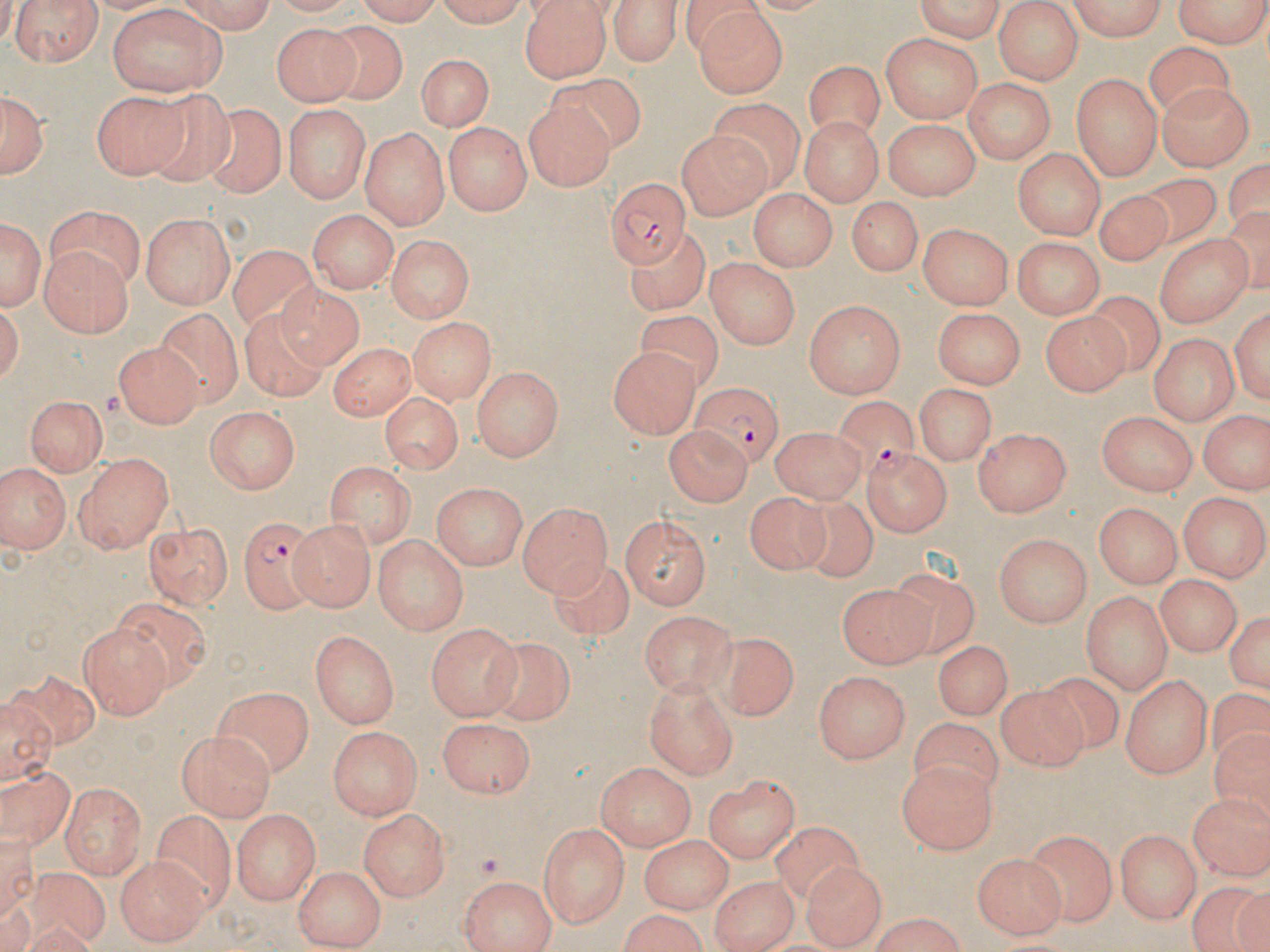 Approximate bounding boxes as [x1, y1, x2, y2] in pixels. Plasmodium falciparum-infected red blood cell locations: [604, 177, 691, 267], [691, 380, 782, 463], [835, 397, 930, 486], [855, 443, 951, 534], [238, 514, 317, 614]. Uninfected red blood cell locations: [6, 0, 106, 67], [172, 0, 278, 32], [349, 0, 451, 23], [429, 0, 531, 26], [519, 0, 610, 83], [607, 0, 686, 65], [906, 0, 1009, 41], [1060, 0, 1168, 41], [995, 1, 1080, 83], [1168, 1, 1270, 49], [692, 4, 788, 97], [107, 5, 226, 96], [315, 24, 408, 104], [270, 25, 356, 108], [882, 35, 980, 124], [1146, 45, 1235, 126], [416, 52, 492, 133], [805, 54, 884, 133], [543, 72, 652, 149], [1072, 74, 1164, 181], [963, 77, 1055, 164], [1157, 81, 1252, 173], [2, 87, 47, 178], [94, 90, 189, 180], [150, 91, 237, 190], [524, 95, 615, 192], [710, 98, 807, 195], [283, 103, 369, 204], [201, 105, 289, 203], [802, 117, 885, 205], [884, 118, 980, 200], [445, 121, 529, 216], [359, 126, 450, 225], [674, 129, 773, 217], [1015, 149, 1105, 239], [1144, 171, 1219, 248], [750, 190, 837, 270], [1091, 191, 1173, 266], [845, 199, 920, 279], [44, 203, 145, 288], [308, 210, 398, 295], [1, 213, 44, 311], [140, 216, 235, 309], [918, 224, 1015, 311], [1152, 234, 1256, 329], [386, 235, 475, 321], [626, 235, 714, 316], [1015, 237, 1104, 316], [227, 245, 327, 340], [39, 248, 132, 337], [706, 259, 803, 348], [277, 276, 377, 372], [1084, 291, 1174, 376], [803, 299, 901, 397], [1231, 301, 1269, 414], [240, 302, 328, 405], [932, 305, 1027, 388], [156, 310, 246, 406], [637, 311, 725, 396], [1039, 313, 1127, 396], [409, 317, 492, 404], [1148, 333, 1239, 423], [327, 339, 418, 418], [113, 344, 199, 429], [606, 345, 702, 437], [472, 366, 563, 461], [912, 382, 993, 464], [377, 392, 466, 471], [24, 393, 107, 478], [206, 406, 298, 495], [1097, 411, 1198, 495], [1200, 412, 1265, 494], [664, 424, 749, 507], [769, 428, 869, 500], [973, 428, 1072, 518], [72, 452, 178, 553], [2, 461, 70, 554], [328, 462, 417, 550], [428, 483, 529, 569], [1179, 491, 1267, 581], [746, 494, 833, 577], [794, 494, 878, 584], [517, 501, 612, 595], [1095, 501, 1182, 586], [620, 511, 714, 611], [145, 520, 233, 608], [290, 520, 372, 611], [994, 532, 1090, 626], [374, 536, 468, 637], [552, 554, 636, 639], [887, 571, 977, 660], [1154, 571, 1239, 660], [840, 578, 936, 667], [1083, 590, 1170, 695], [119, 599, 209, 693], [1228, 608, 1270, 697], [639, 611, 738, 692], [77, 623, 170, 719], [428, 624, 520, 719], [309, 631, 401, 730], [709, 634, 792, 719], [477, 635, 574, 729], [934, 635, 1012, 720], [814, 671, 911, 766], [1119, 671, 1212, 777], [4, 672, 103, 749], [1037, 675, 1125, 750], [645, 677, 740, 776], [213, 683, 314, 776], [1001, 687, 1093, 773], [0, 693, 56, 780], [436, 716, 537, 797], [912, 718, 1004, 800], [1212, 718, 1270, 833], [329, 726, 421, 821], [177, 733, 275, 819], [895, 762, 997, 853], [595, 763, 695, 851], [0, 764, 76, 859], [703, 771, 800, 864], [59, 782, 144, 875], [1187, 790, 1269, 880], [358, 806, 450, 901], [154, 810, 237, 915], [230, 810, 322, 902], [539, 822, 629, 927], [767, 822, 868, 909], [1115, 828, 1203, 923], [1026, 829, 1117, 926], [640, 835, 735, 909], [974, 852, 1068, 937], [115, 856, 209, 944], [801, 857, 888, 950], [23, 865, 110, 944], [292, 865, 387, 945], [710, 873, 799, 952], [459, 874, 560, 952], [1185, 882, 1270, 952], [860, 916, 975, 951]. Slide-level diagnosis: Plasmodium falciparum. Captured at 1000x magnification. One field of a larger specimen. May-Grünwald-Giemsa-stained preparation. Thin blood film. Optical microscopy. Image is 1270×952 pixels.